Locate every malaria parasite.
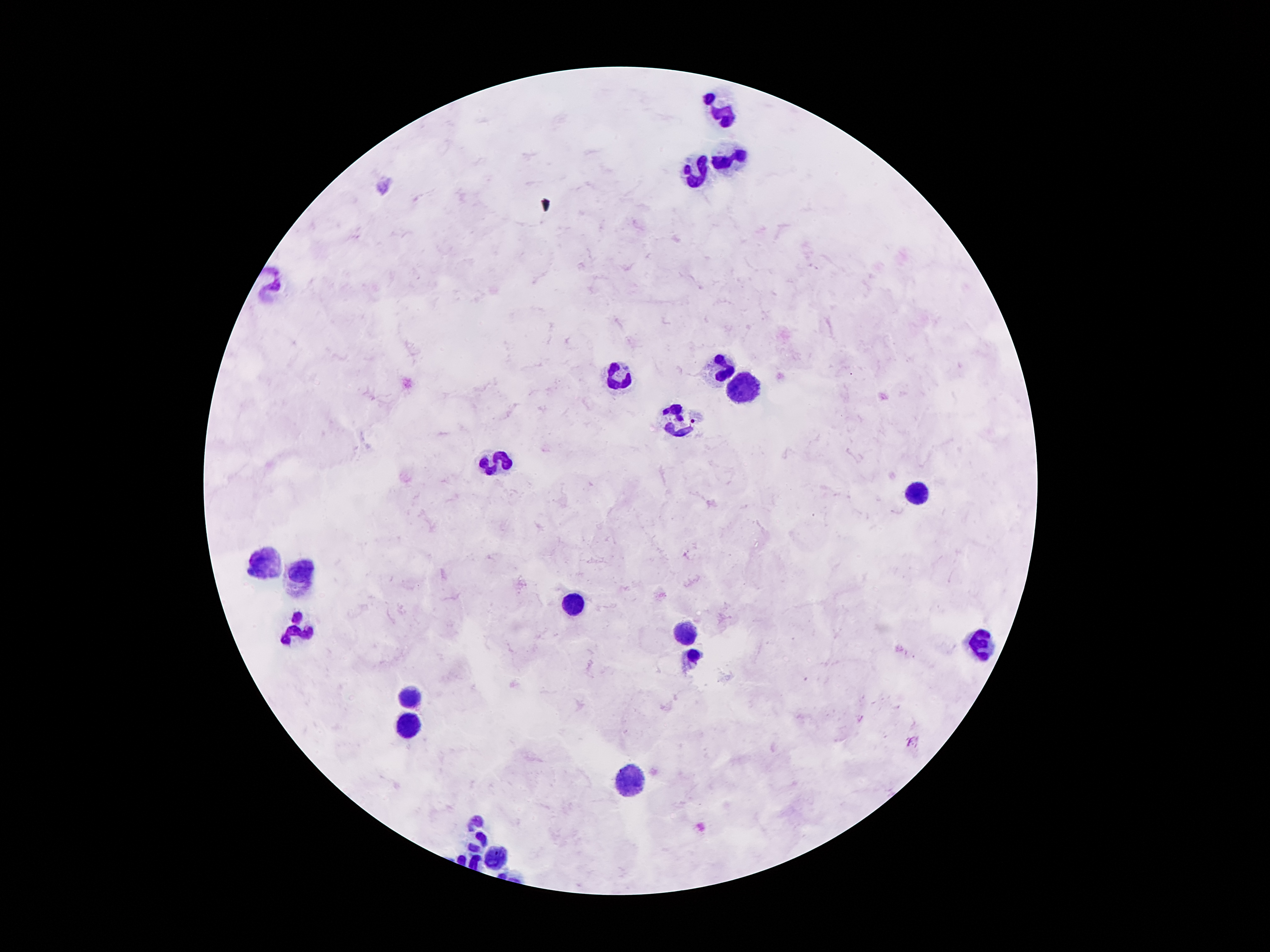
No malaria parasites detected.

coordinate format = approximate object centers, in pixels from the top-left corner
leukocyte locations = (x=721, y=112), (x=729, y=165), (x=692, y=172), (x=722, y=370), (x=617, y=377), (x=743, y=386), (x=679, y=420), (x=491, y=461), (x=917, y=495), (x=267, y=563), (x=301, y=573), (x=570, y=602), (x=298, y=630), (x=679, y=634), (x=982, y=645), (x=694, y=657), (x=411, y=696), (x=405, y=725), (x=629, y=782), (x=475, y=817), (x=479, y=840), (x=494, y=857)
capture = smartphone camera through the microscope eyepiece
magnification = 100x
preparation = thick blood film
patient malaria status = positive for Plasmodium falciparum
field of view = one from this slide
image size = 1270×952 pixels
stain = Giemsa